Name the parasite shown.
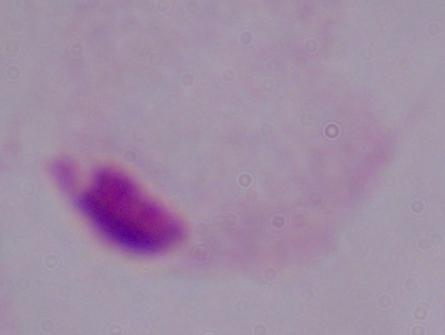

This is a trichomonad.

magnification = 1000x
modality = photomicrograph